Outline each uninfected red blood cell.
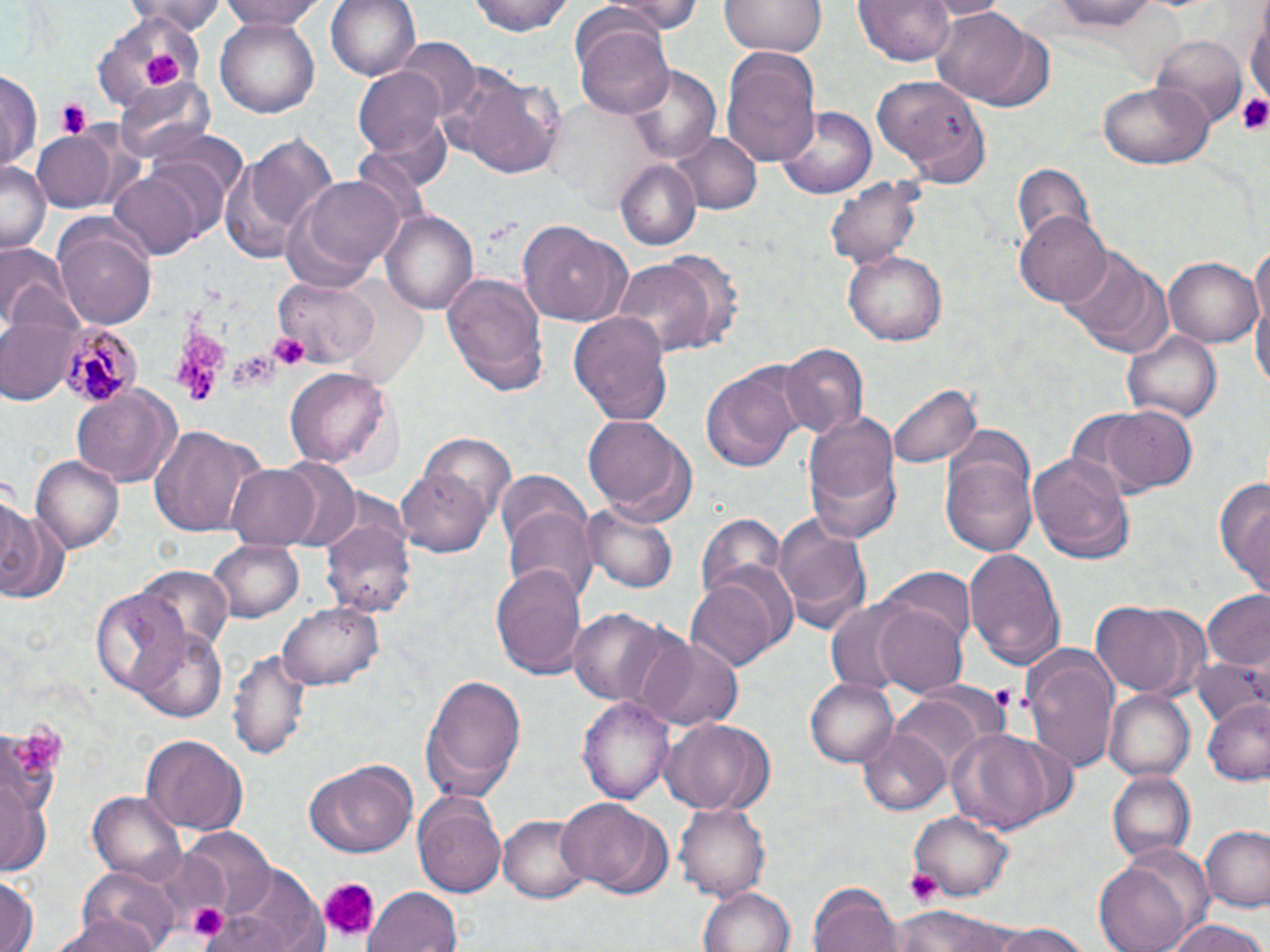

Approximate bounding boxes as named x1/y1/x2/y2 corners in pixels.
Uninfected red blood cells: (x1=219, y1=0, x2=332, y2=27), (x1=326, y1=0, x2=421, y2=82), (x1=470, y1=0, x2=575, y2=36), (x1=601, y1=0, x2=701, y2=38), (x1=721, y1=0, x2=825, y2=58), (x1=856, y1=0, x2=956, y2=67), (x1=1050, y1=0, x2=1165, y2=31), (x1=134, y1=1, x2=227, y2=36), (x1=1244, y1=2, x2=1269, y2=117), (x1=931, y1=7, x2=1038, y2=106), (x1=90, y1=13, x2=204, y2=109), (x1=573, y1=16, x2=677, y2=117), (x1=216, y1=19, x2=320, y2=118), (x1=1150, y1=31, x2=1247, y2=127), (x1=395, y1=37, x2=480, y2=121), (x1=721, y1=47, x2=821, y2=171), (x1=623, y1=64, x2=721, y2=164), (x1=356, y1=66, x2=448, y2=158), (x1=445, y1=70, x2=565, y2=180), (x1=0, y1=71, x2=40, y2=175), (x1=872, y1=75, x2=989, y2=185), (x1=117, y1=77, x2=216, y2=163), (x1=1097, y1=82, x2=1212, y2=171), (x1=774, y1=99, x2=882, y2=199), (x1=31, y1=131, x2=117, y2=213), (x1=226, y1=131, x2=339, y2=264), (x1=673, y1=134, x2=762, y2=214), (x1=615, y1=156, x2=701, y2=250), (x1=0, y1=158, x2=50, y2=251), (x1=1010, y1=163, x2=1098, y2=255), (x1=290, y1=172, x2=406, y2=282), (x1=106, y1=174, x2=202, y2=260), (x1=826, y1=175, x2=925, y2=269), (x1=383, y1=208, x2=479, y2=315), (x1=1015, y1=211, x2=1115, y2=308), (x1=56, y1=222, x2=156, y2=333), (x1=518, y1=222, x2=631, y2=327), (x1=1249, y1=234, x2=1270, y2=350), (x1=2, y1=241, x2=77, y2=337), (x1=1060, y1=246, x2=1168, y2=356), (x1=843, y1=251, x2=945, y2=345), (x1=1164, y1=255, x2=1261, y2=345), (x1=611, y1=258, x2=722, y2=358), (x1=442, y1=272, x2=550, y2=399), (x1=271, y1=277, x2=380, y2=369), (x1=1250, y1=278, x2=1270, y2=409), (x1=1, y1=311, x2=78, y2=404), (x1=569, y1=312, x2=674, y2=425), (x1=1121, y1=327, x2=1224, y2=424), (x1=777, y1=342, x2=868, y2=441), (x1=700, y1=364, x2=807, y2=473), (x1=287, y1=367, x2=393, y2=471), (x1=888, y1=381, x2=980, y2=471), (x1=71, y1=386, x2=182, y2=486), (x1=1100, y1=405, x2=1198, y2=496), (x1=802, y1=410, x2=902, y2=540), (x1=582, y1=414, x2=697, y2=525), (x1=148, y1=424, x2=263, y2=537), (x1=415, y1=430, x2=518, y2=532), (x1=939, y1=449, x2=1038, y2=559), (x1=1029, y1=450, x2=1135, y2=564), (x1=32, y1=455, x2=124, y2=552), (x1=226, y1=463, x2=321, y2=549), (x1=397, y1=464, x2=496, y2=558), (x1=495, y1=472, x2=593, y2=567), (x1=1215, y1=474, x2=1270, y2=597), (x1=0, y1=497, x2=69, y2=607), (x1=503, y1=504, x2=598, y2=603), (x1=582, y1=504, x2=680, y2=594), (x1=772, y1=508, x2=870, y2=637), (x1=694, y1=513, x2=788, y2=614), (x1=322, y1=515, x2=416, y2=620), (x1=208, y1=538, x2=306, y2=624), (x1=962, y1=546, x2=1067, y2=670), (x1=489, y1=563, x2=591, y2=677), (x1=135, y1=564, x2=233, y2=660), (x1=885, y1=569, x2=974, y2=651), (x1=687, y1=572, x2=781, y2=674), (x1=91, y1=588, x2=190, y2=699), (x1=1200, y1=589, x2=1270, y2=672), (x1=823, y1=595, x2=933, y2=699), (x1=871, y1=601, x2=970, y2=695), (x1=1090, y1=601, x2=1198, y2=698), (x1=278, y1=602, x2=382, y2=689), (x1=568, y1=608, x2=674, y2=706), (x1=132, y1=628, x2=229, y2=723), (x1=638, y1=636, x2=743, y2=731), (x1=1022, y1=645, x2=1120, y2=771), (x1=231, y1=650, x2=311, y2=761), (x1=1189, y1=657, x2=1270, y2=733), (x1=419, y1=673, x2=528, y2=803), (x1=804, y1=677, x2=899, y2=768), (x1=1104, y1=691, x2=1194, y2=784), (x1=890, y1=695, x2=988, y2=777), (x1=578, y1=696, x2=673, y2=805), (x1=1202, y1=698, x2=1270, y2=786), (x1=660, y1=716, x2=775, y2=815), (x1=858, y1=726, x2=952, y2=815), (x1=945, y1=728, x2=1070, y2=833), (x1=143, y1=735, x2=247, y2=832), (x1=303, y1=762, x2=415, y2=859), (x1=1107, y1=772, x2=1193, y2=863), (x1=0, y1=781, x2=49, y2=878), (x1=88, y1=791, x2=188, y2=883), (x1=415, y1=796, x2=508, y2=898), (x1=558, y1=798, x2=665, y2=897), (x1=675, y1=801, x2=769, y2=902), (x1=909, y1=810, x2=1013, y2=902), (x1=498, y1=814, x2=592, y2=903), (x1=1200, y1=825, x2=1270, y2=914), (x1=183, y1=830, x2=277, y2=915), (x1=1093, y1=857, x2=1200, y2=952), (x1=214, y1=866, x2=329, y2=948), (x1=0, y1=873, x2=39, y2=952), (x1=68, y1=874, x2=184, y2=952), (x1=809, y1=881, x2=902, y2=952), (x1=698, y1=884, x2=796, y2=952), (x1=366, y1=889, x2=463, y2=952), (x1=895, y1=906, x2=1022, y2=952), (x1=52, y1=911, x2=166, y2=952), (x1=1162, y1=917, x2=1267, y2=952), (x1=982, y1=924, x2=1093, y2=952).

Platelet locations: (x1=144, y1=50, x2=184, y2=91), (x1=1239, y1=93, x2=1270, y2=135), (x1=54, y1=98, x2=93, y2=140), (x1=173, y1=329, x2=226, y2=402), (x1=269, y1=333, x2=310, y2=370), (x1=231, y1=349, x2=279, y2=394), (x1=987, y1=684, x2=1028, y2=716), (x1=9, y1=725, x2=72, y2=779), (x1=906, y1=868, x2=944, y2=905), (x1=315, y1=876, x2=382, y2=943), (x1=187, y1=905, x2=226, y2=944). Plasmodium malariae-infected red blood cell locations: (x1=57, y1=322, x2=139, y2=407). Slide-level diagnosis: Plasmodium malariae. Image is 1270×952 pixels. May-Grünwald-Giemsa-stained preparation. 1000x magnification. Light microscopy. Thin blood film. Single field of view.